Mark where leukocytes are.
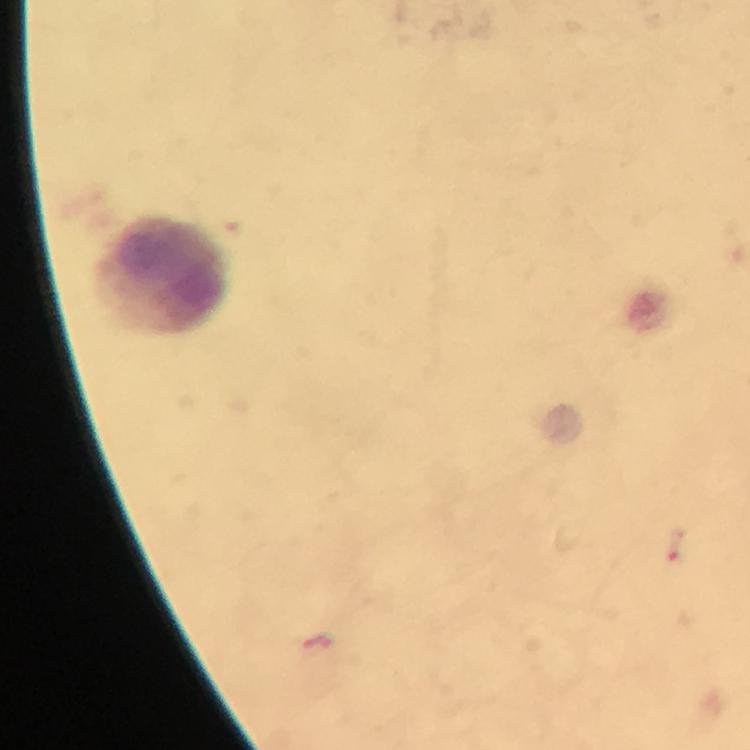

Approximate object centers, in pixels from the top-left corner.
Leukocytes: (x=163, y=275).

Malaria parasite locations: (x=676, y=546). Giemsa stain. Immersion oil applied. From a malaria diagnostic workup. Thick smear. Image is 750×750 pixels. 100x magnification. Photographed through the microscope with a smartphone camera. Cropped region of a single field of view.